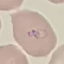 Result: malaria parasites identified. Giemsa stain. Automatically extracted cell patch, resized to 64 × 64 pixels. Thin blood film. Acquired by smartphone through the microscope eyepiece.